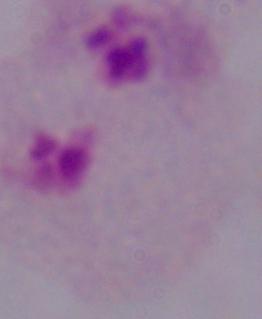
Summary:
  - Identification: trichomonad
  - Modality: micrograph
  - Magnification: 1000x